Comment on the morphology of the red blood cells.
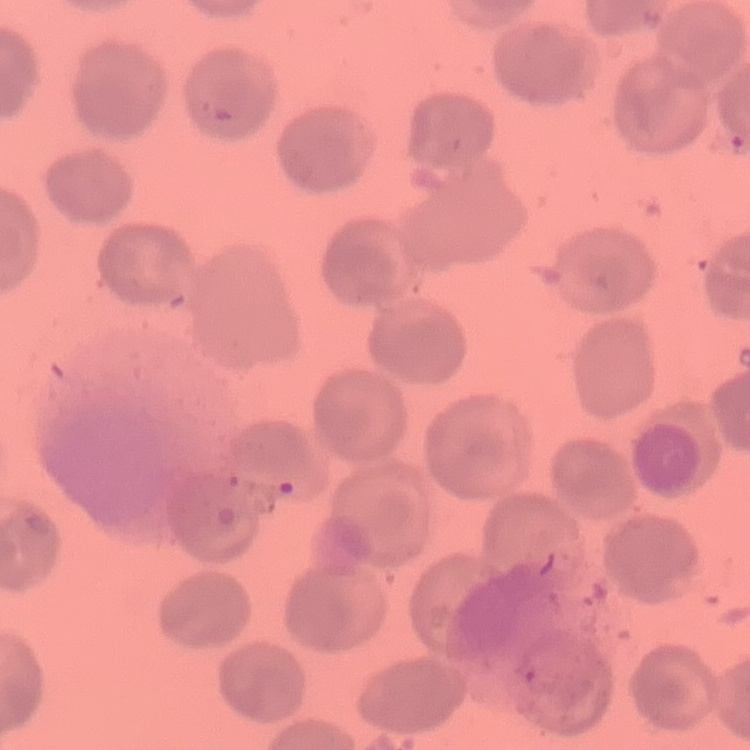

They show no rouleaux formation.

preparation = thin peripheral smear
stain = Field's or Giemsa
image type = one tile cut from a larger photomicrograph